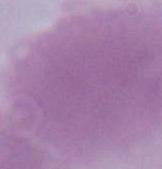
Summary:
  - Magnification: 1000x
  - Modality: micrograph
  - Identification: erythrocyte